Identify the cell.
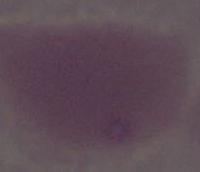

An erythrocyte.

Summary:
  - Modality: micrograph
  - Magnification: 1000x